Identify the blood parasite species.
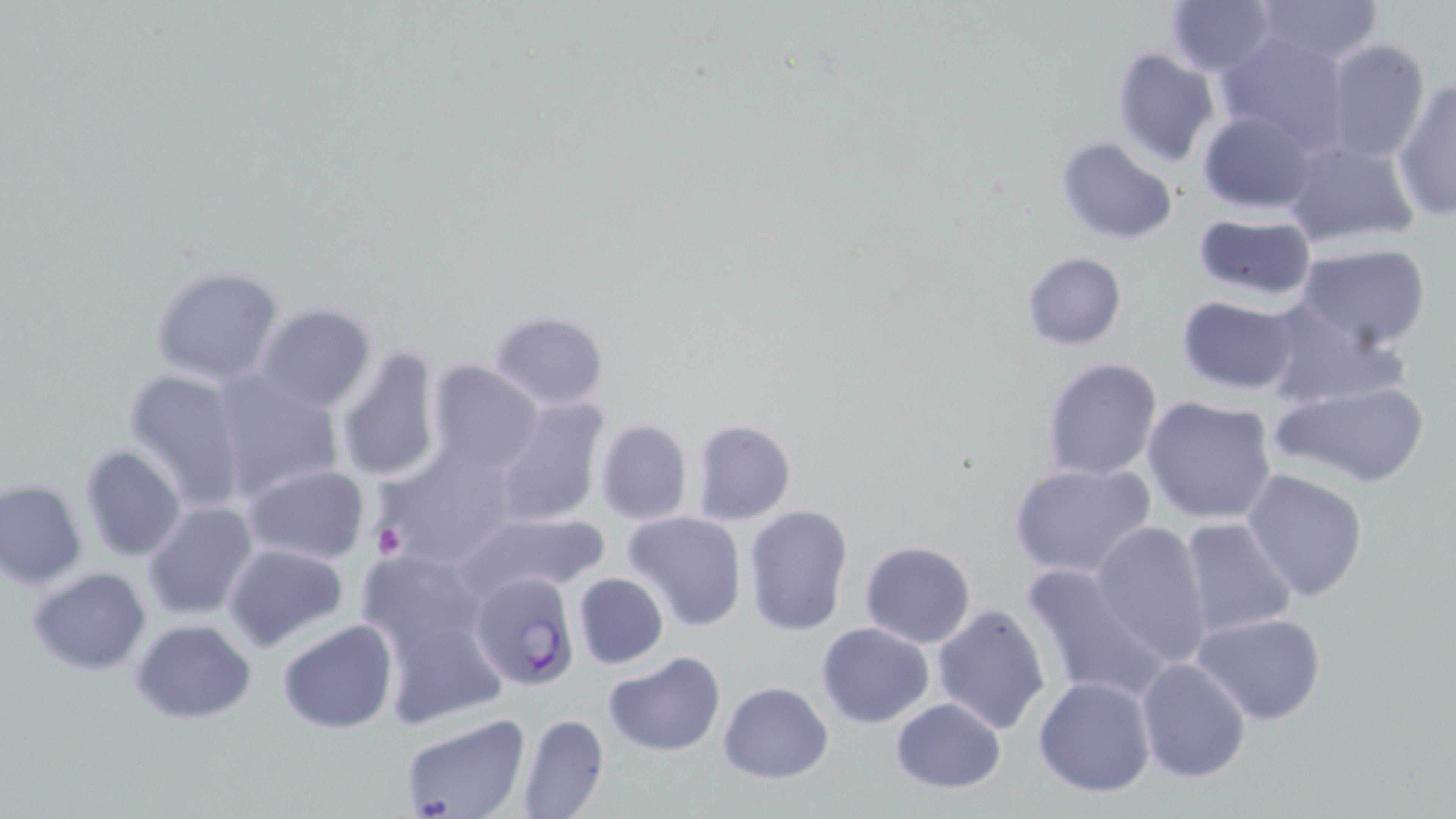

Plasmodium falciparum.

Approximate bounding boxes as (x1,y1)-(x2,y2) corner pairs in pixels. Platelet locations: (372,522)-(408,559). Uninfected red blood cell locations: (1165,0)-(1276,76), (1255,1)-(1385,64), (1215,32)-(1352,153), (1323,39)-(1430,164), (1112,48)-(1220,167), (1392,81)-(1456,220), (1197,111)-(1318,214), (1057,137)-(1178,244), (1281,137)-(1421,250), (1191,213)-(1317,301), (1294,243)-(1434,351), (1021,251)-(1127,350), (149,266)-(286,387), (1177,296)-(1301,395), (1260,301)-(1411,412), (253,303)-(376,414), (490,309)-(609,410), (336,347)-(443,485), (221,355)-(440,490), (1041,356)-(1163,481), (427,359)-(544,476), (123,369)-(251,512), (207,369)-(343,503), (1271,379)-(1431,488), (492,395)-(609,527), (1143,395)-(1277,523), (596,418)-(693,524), (692,419)-(795,525), (79,444)-(186,563), (379,444)-(521,564), (1008,461)-(1157,581), (243,463)-(371,566), (1241,468)-(1368,601), (0,479)-(87,588), (143,502)-(260,620), (743,504)-(854,636), (452,509)-(610,601), (623,512)-(748,631), (1177,518)-(1298,641), (1090,520)-(1213,664), (860,541)-(977,648), (222,543)-(349,653), (355,547)-(489,660), (1020,560)-(1171,703), (28,567)-(151,675), (573,572)-(669,669), (931,604)-(1053,735), (1192,612)-(1328,725), (381,613)-(509,730), (130,618)-(256,723), (277,620)-(399,734), (816,623)-(934,729), (604,652)-(726,758), (1136,658)-(1252,784), (1032,674)-(1158,798), (717,682)-(834,782), (889,697)-(1007,792), (398,711)-(530,819), (518,712)-(608,819). Plasmodium falciparum-infected red blood cell locations: (470,571)-(578,691). Image is 1456×819 pixels. May-Grünwald-Giemsa-stained preparation. Light microscopy. Captured at 1000x magnification. Single field of view. Thin blood film.